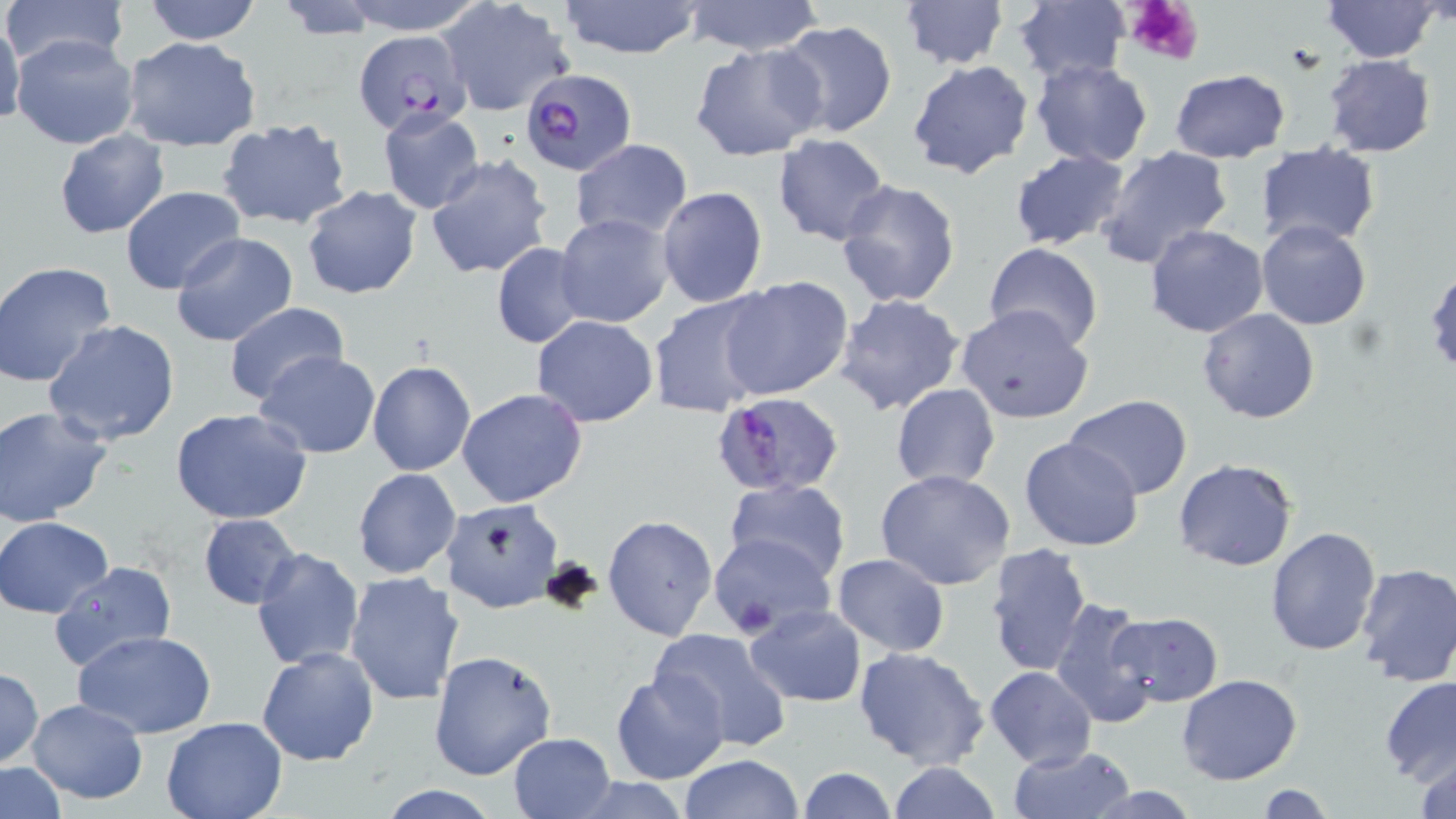
slide-level diagnosis = Plasmodium falciparum
image size = 1456×819 pixels
preparation = thin blood smear
stain = May-Grünwald-Giemsa
platelet locations = approximate bounding boxes as [x1, y1, x2, y2] in pixels: [1123, 0, 1206, 68]
Plasmodium falciparum-infected red blood cell locations = approximate bounding boxes as [x1, y1, x2, y2] in pixels: [352, 30, 474, 135], [521, 68, 636, 175], [708, 396, 840, 500]
uninfected red blood cell locations = approximate bounding boxes as [x1, y1, x2, y2] in pixels: [0, 0, 132, 69], [141, 0, 263, 45], [331, 0, 491, 33], [682, 0, 826, 56], [898, 0, 1007, 71], [1323, 0, 1440, 62], [438, 1, 576, 116], [556, 1, 707, 61], [1010, 3, 1130, 83], [0, 15, 24, 131], [775, 20, 899, 141], [10, 34, 139, 151], [121, 37, 262, 153], [689, 42, 828, 161], [1323, 54, 1435, 157], [1029, 58, 1154, 168], [907, 59, 1034, 179], [1169, 69, 1290, 160], [377, 107, 486, 214], [215, 119, 352, 231], [55, 129, 170, 240], [771, 133, 891, 246], [570, 140, 693, 239], [1256, 142, 1381, 247], [1093, 145, 1235, 269], [1010, 149, 1133, 252], [425, 154, 553, 279], [834, 179, 962, 309], [302, 185, 422, 301], [119, 186, 248, 296], [656, 186, 768, 309], [555, 213, 674, 327], [1256, 220, 1372, 331], [1144, 224, 1269, 338], [171, 231, 298, 348], [983, 242, 1104, 352], [491, 243, 588, 346], [1, 261, 118, 390], [1425, 268, 1456, 380], [720, 276, 853, 400], [647, 294, 773, 417], [834, 294, 963, 416], [222, 302, 350, 407], [956, 305, 1094, 423], [1197, 307, 1322, 424], [530, 314, 658, 426], [42, 320, 183, 446], [254, 350, 382, 457], [367, 360, 476, 476], [890, 383, 1000, 490], [457, 388, 588, 509], [1065, 395, 1194, 498], [0, 404, 113, 527], [169, 409, 314, 527], [1020, 438, 1144, 552], [1171, 458, 1297, 571], [353, 468, 460, 579], [875, 470, 1018, 591], [725, 479, 851, 585], [438, 500, 564, 613], [197, 514, 304, 610], [601, 515, 717, 641], [1, 516, 116, 617], [1264, 526, 1382, 655], [707, 534, 833, 636], [985, 541, 1093, 677], [250, 547, 364, 672], [831, 553, 950, 657], [48, 560, 177, 671], [1354, 563, 1456, 687], [344, 571, 466, 708], [1049, 599, 1159, 728], [743, 603, 867, 707], [1108, 613, 1223, 707], [647, 628, 795, 753], [72, 629, 217, 740], [853, 645, 990, 769], [256, 648, 379, 766], [428, 648, 558, 781], [985, 666, 1097, 769], [0, 667, 44, 767], [611, 669, 728, 785], [1381, 674, 1456, 785], [1176, 675, 1303, 786], [26, 699, 148, 803], [161, 714, 288, 819], [508, 731, 616, 817], [1008, 744, 1132, 819], [1411, 750, 1456, 819], [679, 754, 804, 818], [889, 762, 1002, 819], [1, 763, 67, 817], [796, 767, 897, 819], [565, 776, 698, 817], [374, 783, 505, 818], [1256, 784, 1335, 819]
magnification = 1000x
field of view = single
modality = optical microscopy